Classify this cell by malaria status.
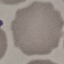
It is uninfected.

Giemsa-stained preparation. Photographed with a smartphone camera at the microscope eyepiece. Cell patch, automatically extracted from a larger field of view and resized to 64 × 64 pixels. Thin blood film.